Report the malaria status of this cell.
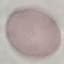
Uninfected.

preparation = thin smear
image type = automatically extracted cell patch, resized to 64 × 64 pixels
stain = Giemsa
capture = smartphone through the microscope eyepiece